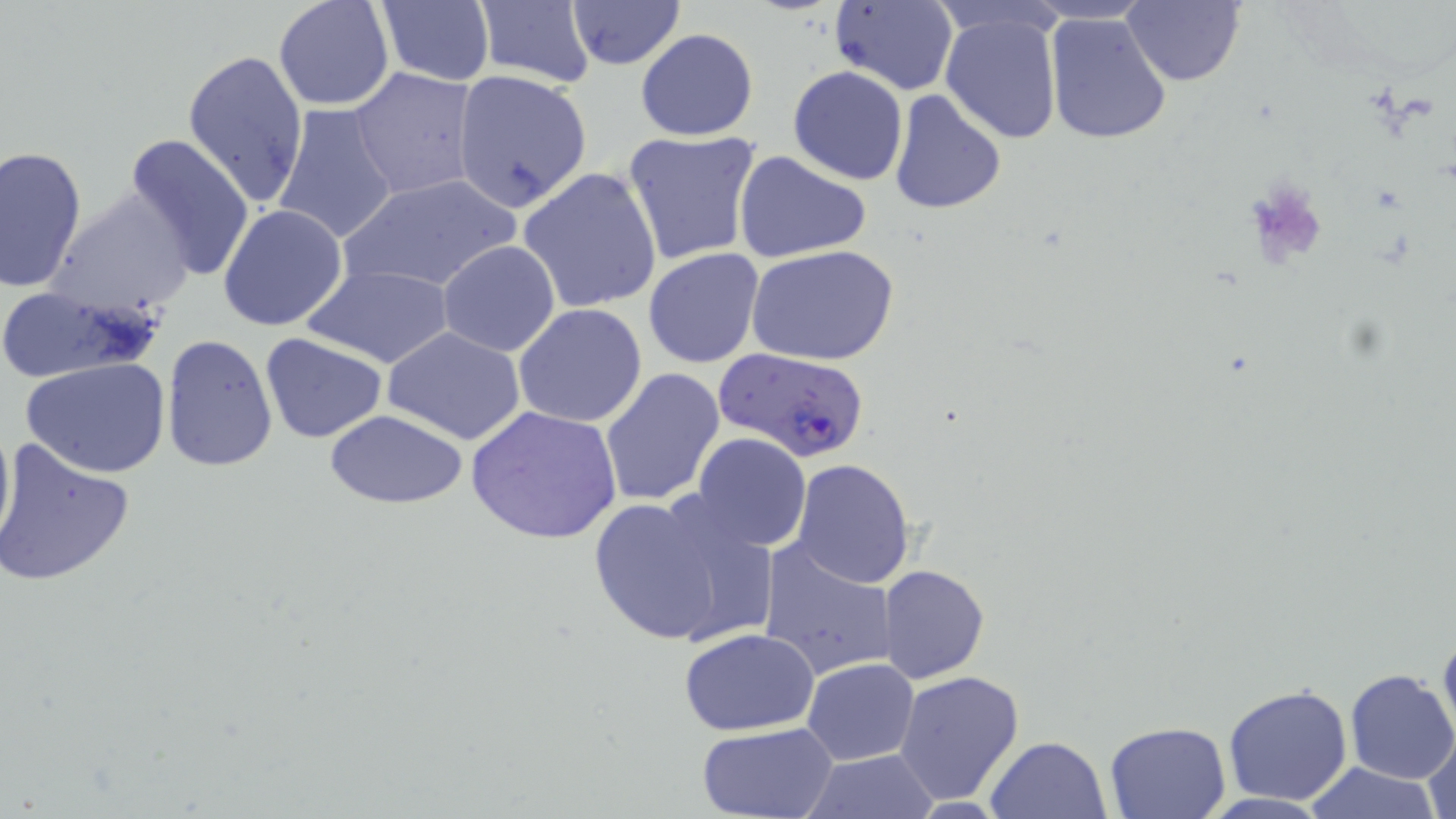

Plasmodium falciparum-infected red blood cell locations = approximate bounding boxes as (x1, y1, x2, y2) in pixels: (712, 348, 871, 462)
slide-level diagnosis = Plasmodium falciparum
stain = May-Grünwald-Giemsa
modality = optical microscopy
uninfected red blood cell locations = approximate bounding boxes as (x1, y1, x2, y2) in pixels: (273, 0, 395, 111), (473, 0, 596, 87), (566, 0, 686, 70), (374, 1, 496, 88), (828, 1, 959, 94), (1122, 1, 1244, 87), (940, 10, 1062, 146), (1043, 12, 1173, 145), (635, 28, 759, 142), (182, 48, 310, 209), (787, 65, 909, 185), (350, 67, 480, 201), (452, 69, 591, 213), (887, 88, 1007, 217), (274, 104, 401, 246), (622, 129, 761, 267), (122, 132, 256, 282), (0, 145, 87, 295), (732, 149, 872, 265), (518, 166, 663, 314), (340, 173, 523, 296), (48, 189, 197, 319), (218, 203, 348, 333), (437, 239, 562, 357), (749, 244, 899, 367), (642, 248, 766, 369), (303, 265, 453, 369), (0, 283, 164, 382), (513, 303, 647, 429), (383, 326, 527, 445), (162, 333, 278, 474), (258, 333, 389, 444), (22, 358, 171, 479), (599, 367, 726, 507), (466, 405, 626, 547), (323, 410, 471, 508), (0, 411, 15, 556), (693, 432, 811, 551), (1, 439, 137, 588), (789, 458, 917, 589), (585, 489, 769, 648), (757, 542, 897, 683), (878, 564, 989, 684), (1437, 624, 1456, 746), (679, 627, 821, 737), (802, 658, 920, 765), (894, 670, 1025, 805), (1344, 670, 1456, 784), (1222, 682, 1353, 806), (696, 720, 842, 819), (1105, 721, 1232, 819), (1423, 731, 1455, 819), (985, 736, 1112, 819), (798, 748, 941, 818), (1299, 761, 1444, 818)
magnification = 1000x
image size = 1456×819 pixels
preparation = thin blood film
field of view = single